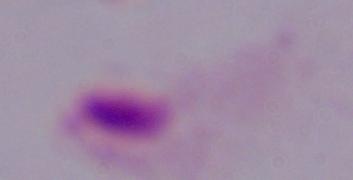
modality = micrograph
magnification = 1000x
identification = trichomonad